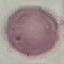
Summary:
  - Malaria status: uninfected
  - Image type: cell patch, automatically extracted from a larger field of view and resized to 64 × 64 pixels
  - Preparation: thin blood film
  - Capture: smartphone camera at the microscope eyepiece
  - Stain: Giemsa